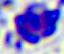 A white blood cell is shown. 400x magnification. Micrograph.